Describe the morphology of the erythrocytes.
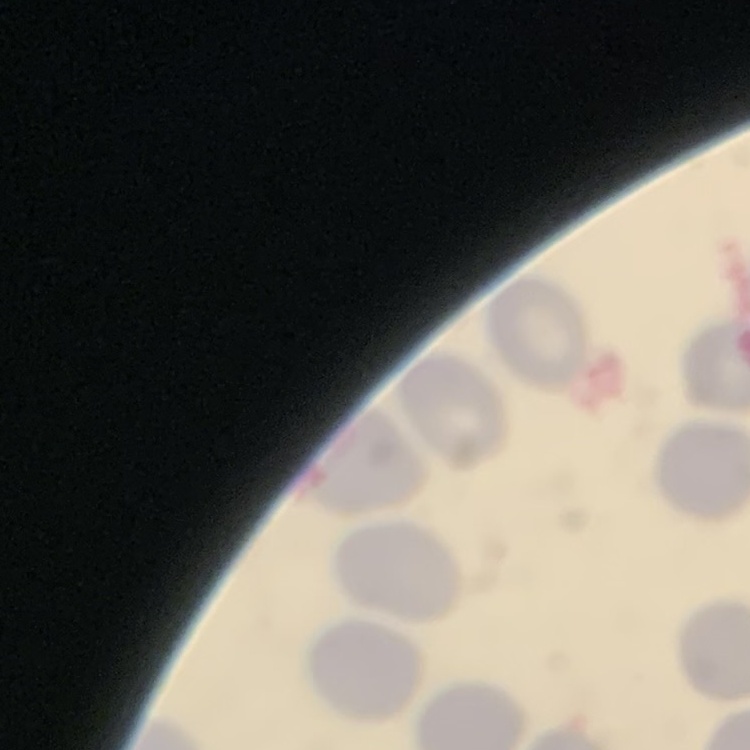

They show no rouleaux formation.

image_type: one tile cut from a larger photomicrograph
stain: Field's or Giemsa
preparation: thin blood smear